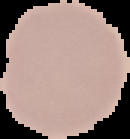
image type = segmented cell region with the area outside set to black
malaria status = uninfected
preparation = thin blood film
image size = 130×139 pixels